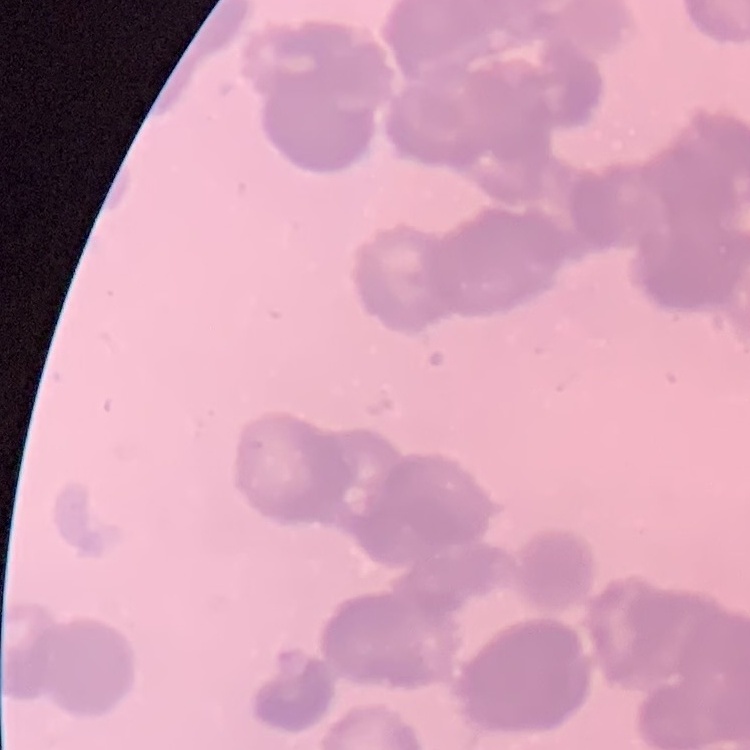
The erythrocytes show rouleaux formation. One tile cut from a larger photomicrograph. Stained with either Field's or Giemsa. Thin blood film.